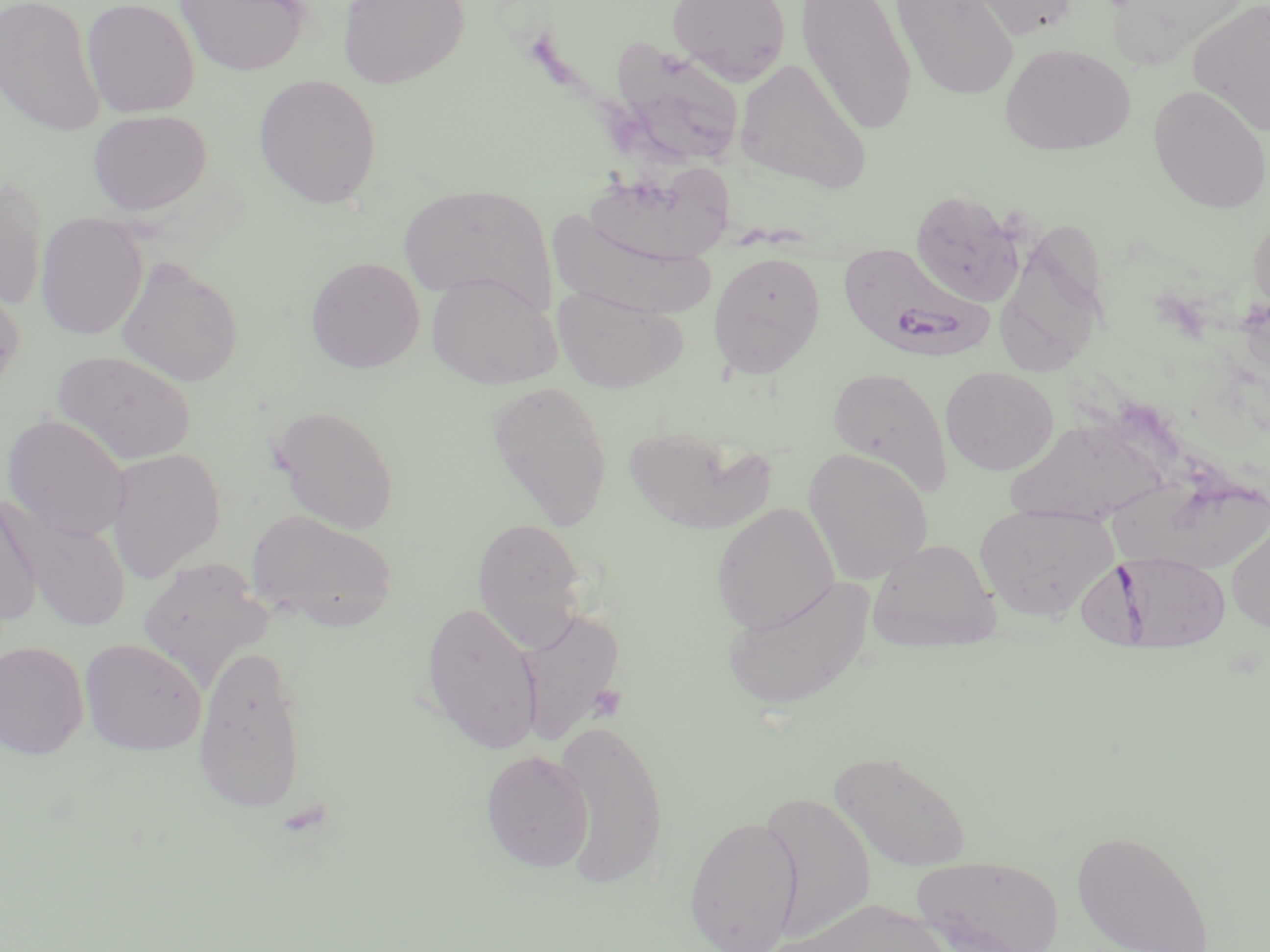

Summary:
  - Coordinate format: approximate bounding boxes as named x1/y1/x2/y2 corners in pixels
  - Uninfected red blood cell locations: (x1=0, y1=0, x2=105, y2=137), (x1=81, y1=0, x2=200, y2=117), (x1=176, y1=0, x2=309, y2=76), (x1=337, y1=0, x2=470, y2=89), (x1=667, y1=0, x2=792, y2=84), (x1=797, y1=0, x2=917, y2=136), (x1=889, y1=0, x2=1021, y2=102), (x1=957, y1=0, x2=1080, y2=40), (x1=1189, y1=0, x2=1270, y2=136), (x1=1107, y1=2, x2=1246, y2=75), (x1=611, y1=41, x2=746, y2=167), (x1=999, y1=42, x2=1136, y2=156), (x1=734, y1=56, x2=872, y2=194), (x1=253, y1=74, x2=382, y2=209), (x1=1148, y1=84, x2=1270, y2=213), (x1=87, y1=109, x2=212, y2=215), (x1=580, y1=158, x2=746, y2=269), (x1=0, y1=172, x2=49, y2=313), (x1=397, y1=184, x2=556, y2=314), (x1=908, y1=188, x2=1026, y2=306), (x1=35, y1=212, x2=148, y2=340), (x1=547, y1=212, x2=718, y2=320), (x1=1248, y1=213, x2=1270, y2=317), (x1=996, y1=221, x2=1113, y2=382), (x1=707, y1=251, x2=826, y2=377), (x1=305, y1=256, x2=425, y2=374), (x1=115, y1=258, x2=245, y2=387), (x1=426, y1=272, x2=561, y2=389), (x1=0, y1=280, x2=26, y2=398), (x1=551, y1=284, x2=687, y2=394), (x1=52, y1=349, x2=196, y2=465), (x1=940, y1=365, x2=1058, y2=475), (x1=827, y1=366, x2=953, y2=498), (x1=486, y1=380, x2=613, y2=529), (x1=269, y1=404, x2=399, y2=534), (x1=2, y1=413, x2=132, y2=542), (x1=1005, y1=417, x2=1171, y2=526), (x1=623, y1=424, x2=776, y2=534), (x1=105, y1=447, x2=226, y2=582), (x1=802, y1=447, x2=933, y2=585), (x1=1104, y1=476, x2=1270, y2=574), (x1=0, y1=492, x2=44, y2=630), (x1=711, y1=502, x2=839, y2=635), (x1=974, y1=503, x2=1117, y2=622), (x1=4, y1=505, x2=132, y2=633), (x1=248, y1=509, x2=398, y2=632), (x1=471, y1=517, x2=589, y2=650), (x1=1226, y1=518, x2=1270, y2=633), (x1=867, y1=538, x2=1000, y2=651), (x1=137, y1=558, x2=272, y2=690), (x1=720, y1=574, x2=875, y2=712), (x1=420, y1=602, x2=543, y2=753), (x1=514, y1=607, x2=626, y2=747), (x1=79, y1=638, x2=207, y2=755), (x1=0, y1=640, x2=89, y2=759), (x1=192, y1=644, x2=308, y2=815), (x1=553, y1=718, x2=669, y2=887), (x1=480, y1=750, x2=594, y2=872), (x1=829, y1=750, x2=972, y2=873), (x1=759, y1=790, x2=876, y2=942), (x1=684, y1=814, x2=803, y2=952), (x1=1071, y1=829, x2=1214, y2=952), (x1=913, y1=854, x2=1062, y2=952), (x1=783, y1=899, x2=958, y2=952)
  - Plasmodium falciparum-infected red blood cell locations: (x1=837, y1=241, x2=992, y2=362), (x1=1102, y1=552, x2=1234, y2=644)
  - Slide-level diagnosis: Plasmodium falciparum
  - Field of view: single
  - Preparation: thin blood film
  - Modality: light microscopy
  - Image size: 1270×952 pixels
  - Stain: May-Grünwald-Giemsa
  - Magnification: 1000x